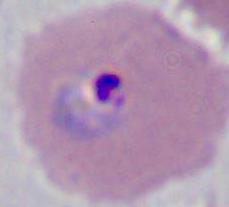

Photomicrograph. 400x or 1000x magnification. A Plasmodium parasite is seen.